Locate leukocytes (white blood cells).
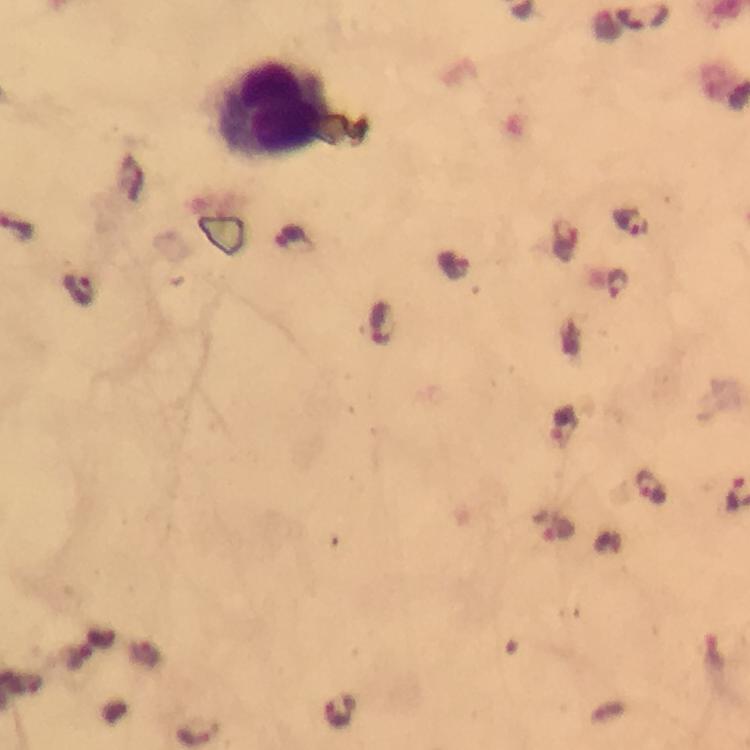

Approximate centers as (x, y) in pixels.
Leukocytes: (276, 110).

Plasmodium parasite locations: (642, 16), (631, 217), (452, 261), (616, 286), (383, 322), (564, 423), (555, 526). Smartphone photograph taken through a microscope. Thick smear. Giemsa-stained preparation. Cropped region of a single field of view. 100x magnification. From a diagnostic examination for malaria. Immersion oil applied. Image is 750×750 pixels.